Report the malaria status of this cell.
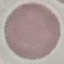
It is uninfected.

stain = Giemsa
image type = automatically extracted cell patch, resized to 64 × 64 pixels
capture = smartphone camera at the microscope eyepiece
preparation = thin smear